Identify the parasite.
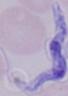
This is a trypanosome.

Summary:
  - Magnification: 1000x
  - Modality: micrograph